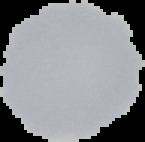

Summary:
  - Preparation: thin blood smear
  - Result: negative for Plasmodium parasites
  - Image size: 145×142 pixels
  - Image type: segmented cell region with the area outside set to black